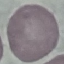
Summary:
  - Malaria status: uninfected
  - Stain: Giemsa
  - Image type: cell patch, automatically extracted from a larger field of view and resized to 64 × 64 pixels
  - Preparation: thin blood film
  - Capture: smartphone through the microscope eyepiece